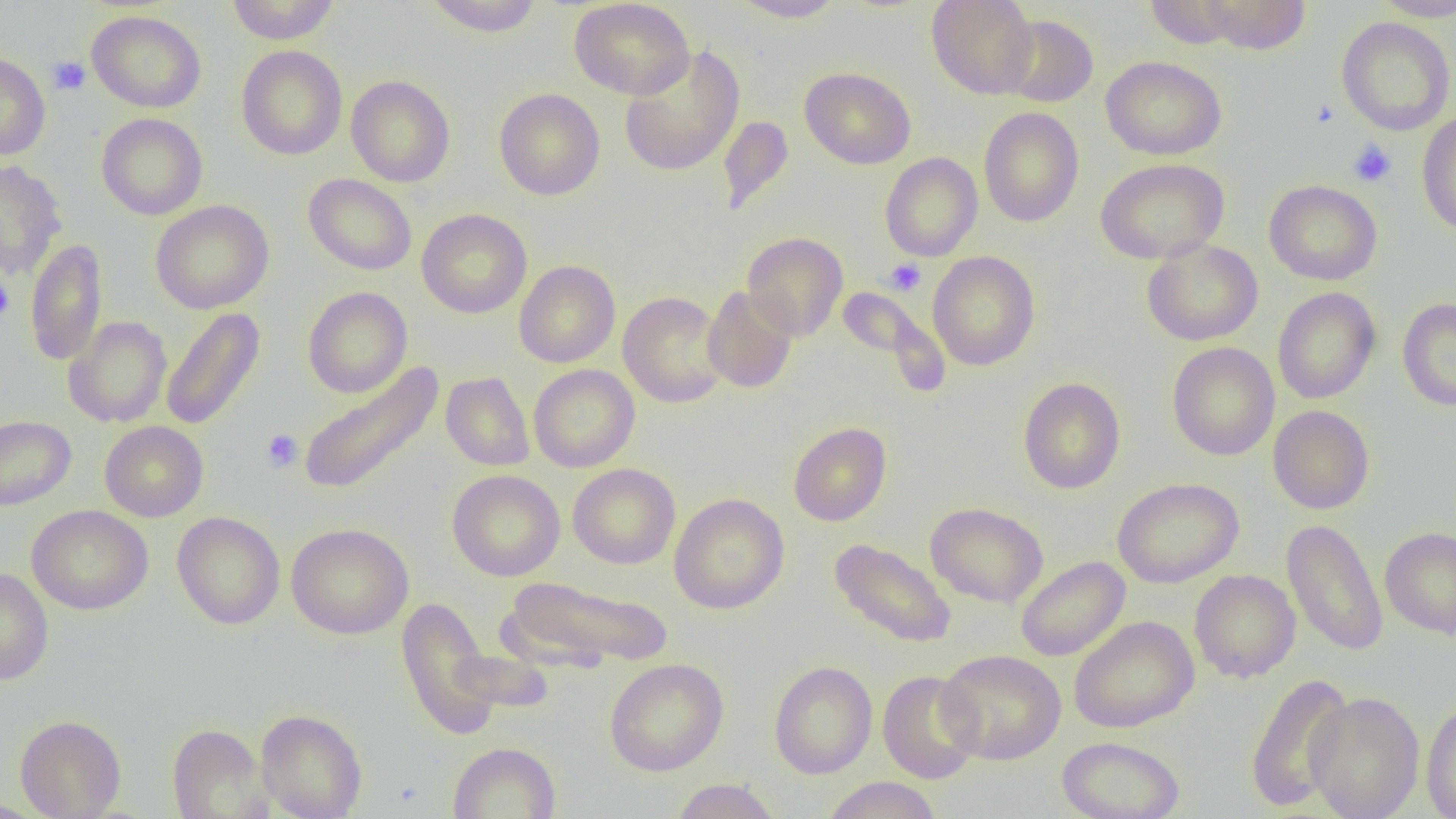
Approximate bounding boxes as named x1/y1/x2/y2 corners in pixels. Platelet locations: (x1=47, y1=56, x2=90, y2=95), (x1=1309, y1=99, x2=1338, y2=128), (x1=1349, y1=139, x2=1396, y2=187), (x1=884, y1=259, x2=926, y2=296), (x1=0, y1=276, x2=14, y2=322), (x1=261, y1=429, x2=303, y2=472). Uninfected red blood cell locations: (x1=227, y1=0, x2=342, y2=44), (x1=424, y1=0, x2=544, y2=37), (x1=569, y1=0, x2=695, y2=100), (x1=729, y1=0, x2=847, y2=23), (x1=926, y1=0, x2=1038, y2=99), (x1=1197, y1=0, x2=1311, y2=55), (x1=1372, y1=0, x2=1456, y2=21), (x1=1146, y1=1, x2=1245, y2=49), (x1=87, y1=11, x2=206, y2=113), (x1=999, y1=14, x2=1098, y2=107), (x1=1336, y1=16, x2=1455, y2=136), (x1=236, y1=45, x2=347, y2=160), (x1=619, y1=46, x2=746, y2=177), (x1=0, y1=52, x2=51, y2=160), (x1=1101, y1=56, x2=1227, y2=160), (x1=800, y1=67, x2=916, y2=169), (x1=346, y1=75, x2=456, y2=187), (x1=494, y1=88, x2=605, y2=201), (x1=979, y1=107, x2=1084, y2=227), (x1=1416, y1=111, x2=1456, y2=236), (x1=96, y1=113, x2=208, y2=220), (x1=717, y1=115, x2=795, y2=216), (x1=880, y1=152, x2=983, y2=261), (x1=1095, y1=158, x2=1229, y2=265), (x1=0, y1=160, x2=67, y2=279), (x1=303, y1=174, x2=417, y2=275), (x1=1264, y1=180, x2=1382, y2=285), (x1=150, y1=200, x2=274, y2=314), (x1=417, y1=209, x2=532, y2=318), (x1=742, y1=232, x2=848, y2=341), (x1=25, y1=238, x2=108, y2=366), (x1=1142, y1=239, x2=1263, y2=346), (x1=928, y1=251, x2=1041, y2=370), (x1=514, y1=260, x2=620, y2=367), (x1=302, y1=286, x2=412, y2=398), (x1=702, y1=286, x2=798, y2=394), (x1=1272, y1=287, x2=1381, y2=404), (x1=836, y1=288, x2=950, y2=395), (x1=618, y1=291, x2=729, y2=408), (x1=1397, y1=297, x2=1456, y2=411), (x1=160, y1=306, x2=265, y2=431), (x1=63, y1=316, x2=172, y2=428), (x1=1167, y1=342, x2=1280, y2=461), (x1=298, y1=361, x2=444, y2=497), (x1=528, y1=364, x2=640, y2=472), (x1=441, y1=372, x2=535, y2=471), (x1=1018, y1=377, x2=1126, y2=494), (x1=1268, y1=405, x2=1375, y2=514), (x1=0, y1=415, x2=76, y2=510), (x1=100, y1=421, x2=208, y2=522), (x1=788, y1=422, x2=892, y2=526), (x1=567, y1=463, x2=681, y2=569), (x1=447, y1=469, x2=565, y2=581), (x1=1113, y1=477, x2=1244, y2=588), (x1=669, y1=493, x2=789, y2=615), (x1=925, y1=502, x2=1049, y2=608), (x1=27, y1=505, x2=153, y2=615), (x1=172, y1=511, x2=285, y2=629), (x1=1281, y1=518, x2=1388, y2=657), (x1=286, y1=522, x2=414, y2=639), (x1=1379, y1=526, x2=1456, y2=639), (x1=829, y1=538, x2=957, y2=649), (x1=1015, y1=556, x2=1130, y2=661), (x1=0, y1=568, x2=54, y2=684), (x1=1189, y1=570, x2=1300, y2=683), (x1=500, y1=574, x2=674, y2=671), (x1=396, y1=596, x2=500, y2=739), (x1=1069, y1=615, x2=1199, y2=733), (x1=936, y1=649, x2=1066, y2=765), (x1=604, y1=659, x2=728, y2=776), (x1=768, y1=661, x2=878, y2=779), (x1=877, y1=670, x2=983, y2=784), (x1=1244, y1=672, x2=1355, y2=812), (x1=1305, y1=691, x2=1424, y2=819), (x1=1421, y1=699, x2=1456, y2=818), (x1=256, y1=709, x2=367, y2=819), (x1=15, y1=714, x2=126, y2=819), (x1=167, y1=724, x2=271, y2=819), (x1=1057, y1=736, x2=1185, y2=819), (x1=447, y1=741, x2=561, y2=819), (x1=821, y1=776, x2=942, y2=819), (x1=670, y1=778, x2=782, y2=819). Slide-level diagnosis: negative for blood parasites. Thin blood smear. Optical microscopy. Image is 1456×819 pixels. 1000x magnification. Single field of view.